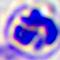

modality: photomicrograph
identification: leukocyte
magnification: 400x